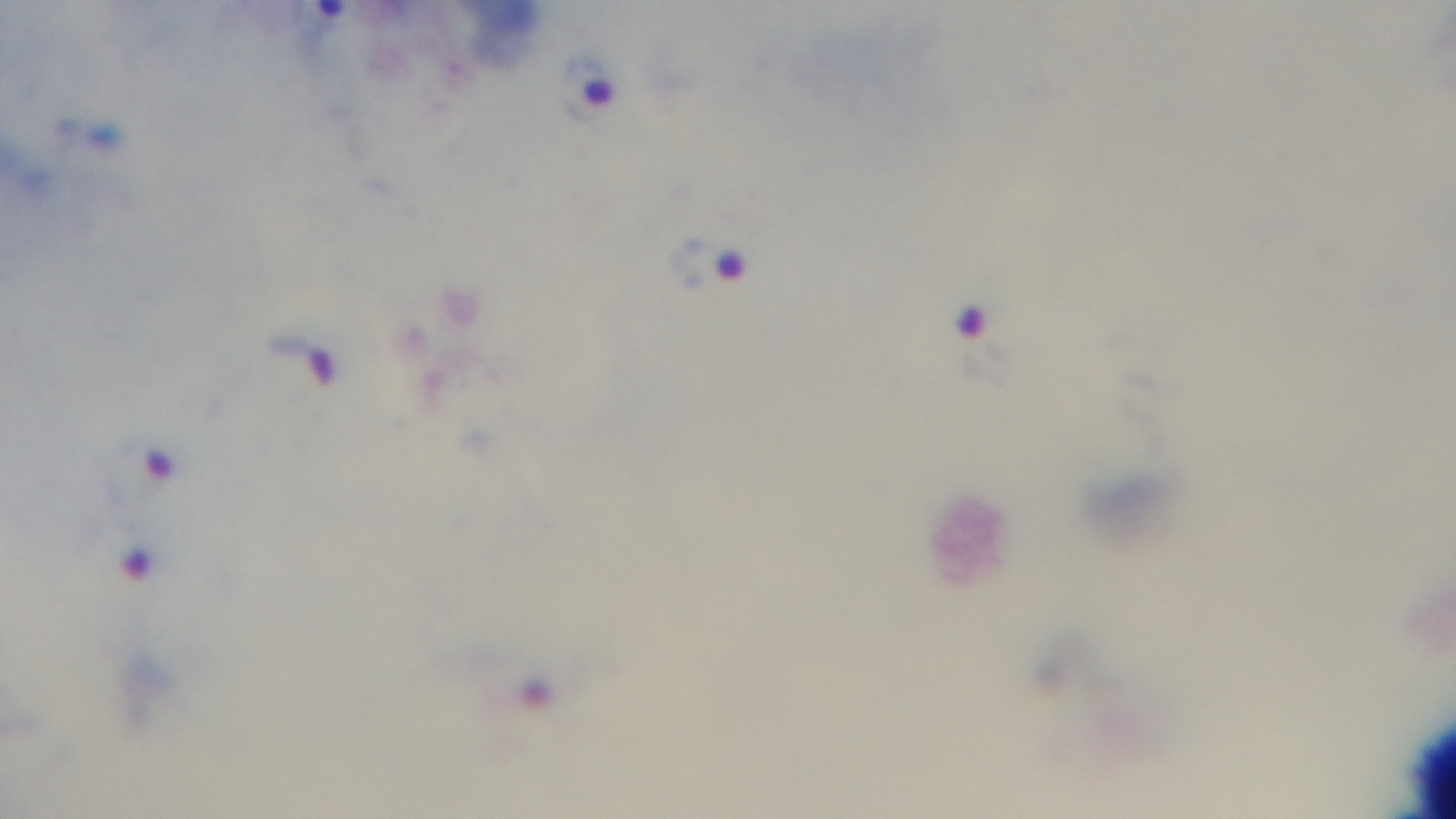
Summary:
  - Malaria status: infected
  - Preparation: thick blood film
  - Field of view: one from the slide
  - Capture: mounted 4K digital camera
  - Stain: Giemsa
  - Objective: 100x oil immersion
  - Modality: light microscopy